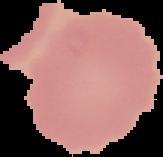
preparation: thin blood smear
image_size: 163×157 pixels
malaria_status: uninfected
image_type: segmented cell region with the area outside set to black